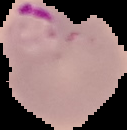
Summary:
  - Preparation: thin blood film
  - Image size: 127×130 pixels
  - Image type: segmented cell region on a black background
  - Result: malaria parasites identified